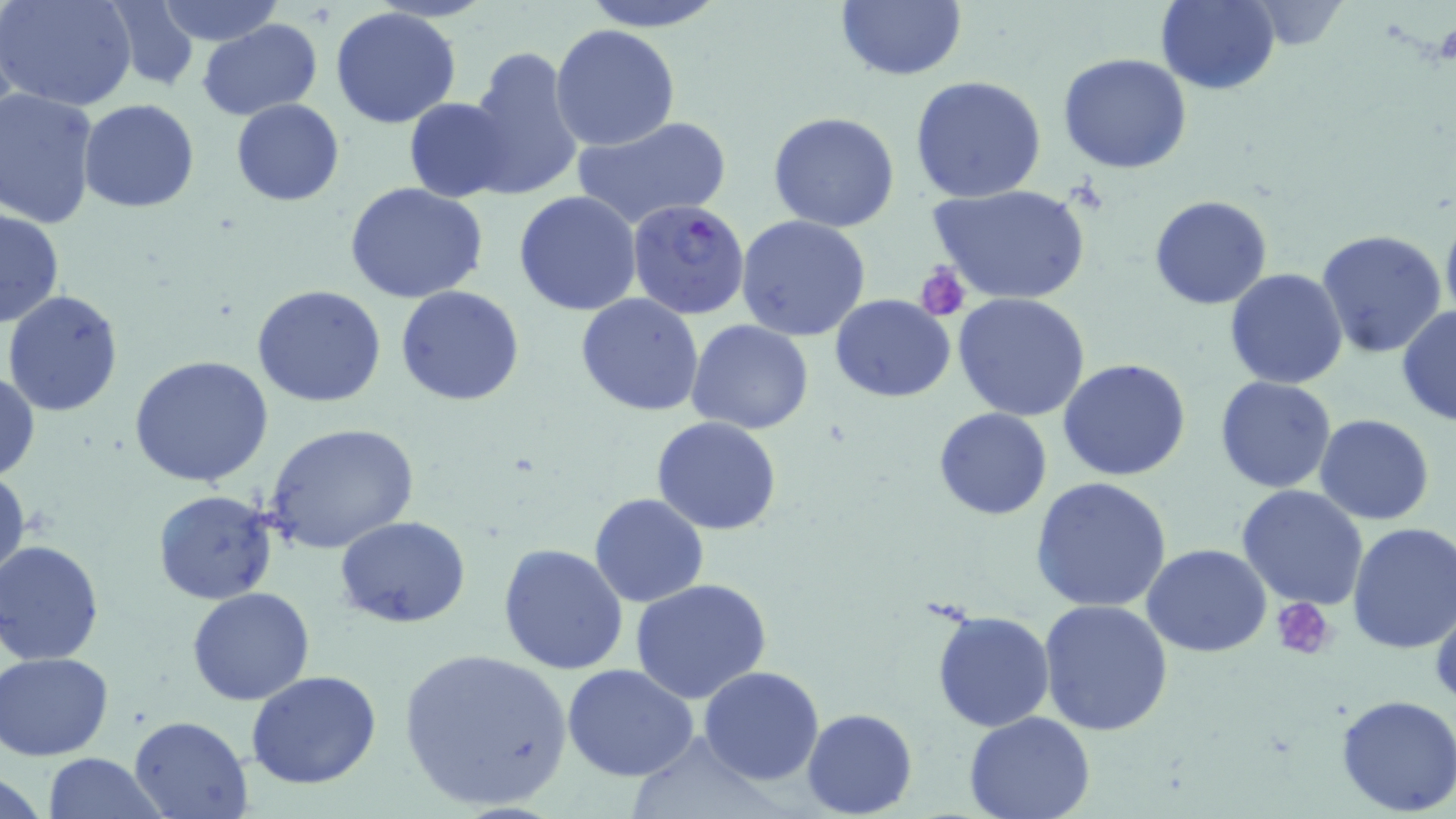

Approximate bounding boxes as (x1,y1)-(x2,y2) corner pairs in pixels. Platelet locations: (916,264)-(970,321), (1272,597)-(1336,657). Uninfected red blood cell locations: (1,0)-(139,112), (156,0)-(284,45), (578,0)-(728,31), (834,0)-(968,82), (1154,1)-(1280,94), (103,3)-(204,90), (330,8)-(463,129), (198,19)-(321,119), (550,24)-(680,152), (465,45)-(584,200), (1057,53)-(1192,174), (909,76)-(1048,204), (0,89)-(99,229), (403,97)-(513,203), (79,99)-(199,214), (231,99)-(344,205), (767,111)-(900,232), (572,115)-(734,230), (344,181)-(488,303), (928,184)-(1091,306), (513,190)-(641,317), (1149,194)-(1274,310), (1440,204)-(1456,330), (0,206)-(65,329), (736,215)-(872,342), (1315,229)-(1449,360), (1225,267)-(1348,389), (251,284)-(387,407), (395,284)-(526,406), (4,289)-(126,415), (576,293)-(705,417), (952,293)-(1091,421), (830,294)-(956,402), (1396,305)-(1455,427), (687,320)-(813,437), (129,354)-(274,488), (1057,359)-(1191,482), (0,370)-(39,483), (1215,376)-(1337,493), (933,407)-(1052,520), (1315,414)-(1436,526), (652,415)-(783,535), (264,422)-(420,554), (0,465)-(28,591), (1030,476)-(1172,614), (1237,484)-(1370,609), (152,490)-(278,605), (590,493)-(708,607), (335,515)-(471,628), (1346,523)-(1456,654), (0,540)-(105,663), (498,543)-(629,675), (1142,544)-(1273,658), (629,577)-(773,703), (186,587)-(315,705), (1039,600)-(1174,739), (931,609)-(1054,730), (394,644)-(575,814), (2,652)-(116,760), (562,665)-(700,783), (698,666)-(824,785), (247,669)-(381,789), (1335,693)-(1456,815), (801,709)-(918,819), (963,709)-(1095,819), (129,714)-(253,817), (41,753)-(170,819). Plasmodium falciparum-infected red blood cell locations: (625,198)-(751,321). Slide-level diagnosis: Plasmodium falciparum. Captured at 1000x magnification. Thin blood film. One field of a larger specimen. Light microscopy. May-Grünwald-Giemsa-stained preparation. Image is 1456×819 pixels.